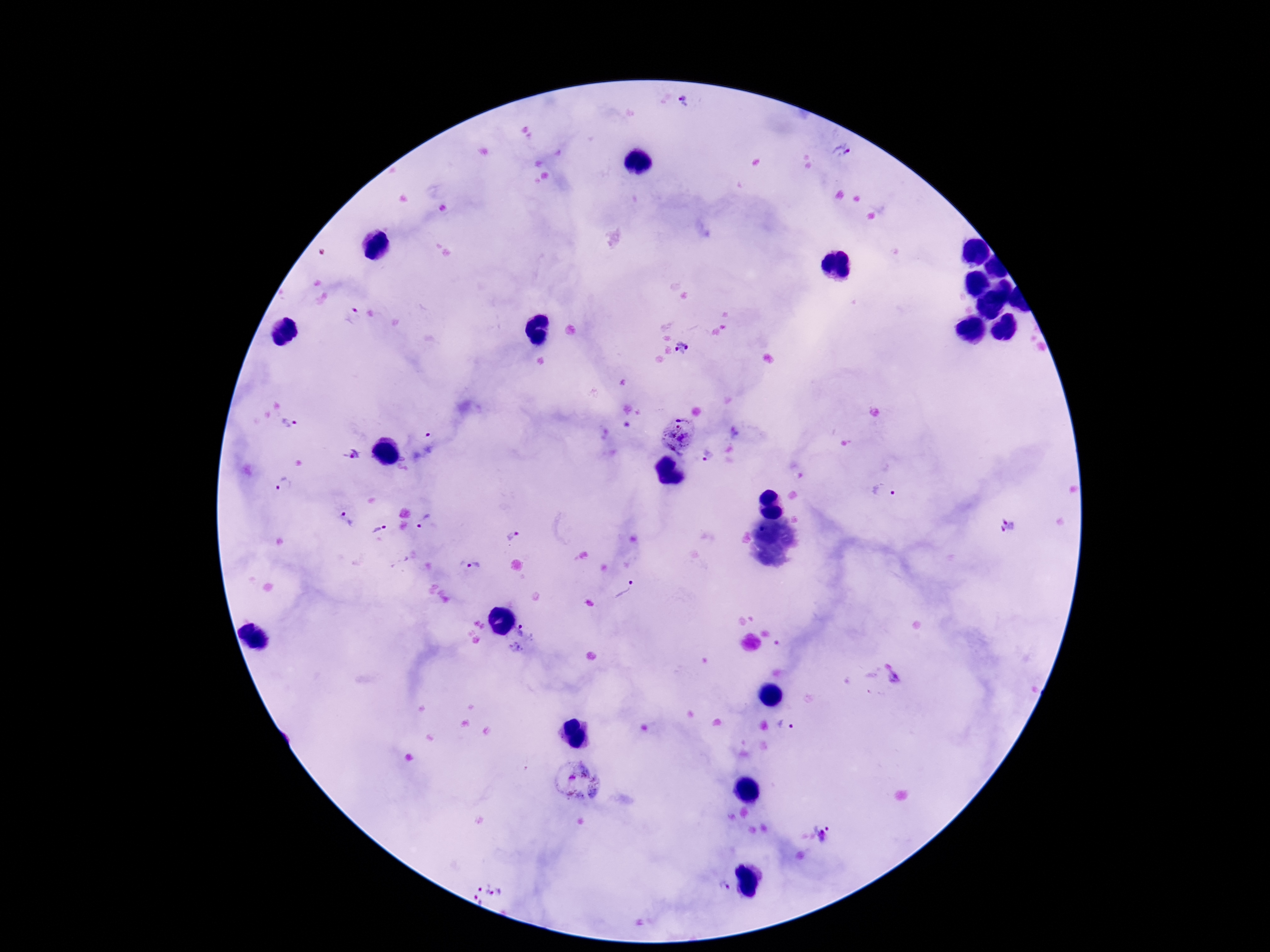
Approximate object centers, in pixels from the top-left corner.
Summary:
  - Plasmodium parasite locations: (x=684, y=102), (x=841, y=151), (x=352, y=316), (x=683, y=349), (x=289, y=423), (x=737, y=432), (x=423, y=434), (x=681, y=435), (x=352, y=454), (x=707, y=455), (x=284, y=484), (x=882, y=492), (x=345, y=520), (x=423, y=521), (x=1010, y=525), (x=379, y=528), (x=512, y=535), (x=473, y=566), (x=627, y=591), (x=519, y=631), (x=516, y=649), (x=895, y=679), (x=786, y=725), (x=580, y=780), (x=824, y=833), (x=724, y=886), (x=488, y=894)
  - Image size: 1270×952 pixels
  - Magnification: 100x
  - Patient malaria status: infected
  - Stain: Giemsa
  - Capture: smartphone camera through the microscope eyepiece
  - Preparation: thick blood film
  - Field of view: one from this slide